Report the malaria status of this cell.
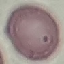

It is uninfected.

Summary:
  - Image type: automatically extracted cell patch, resized to 64 × 64 pixels
  - Stain: Giemsa
  - Capture: smartphone through the microscope eyepiece
  - Preparation: thin smear